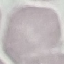

malaria status = uninfected
stain = Giemsa
image type = cell patch, automatically extracted from a larger field of view and resized to 64 × 64 pixels
preparation = thin blood smear
capture = smartphone through the microscope eyepiece